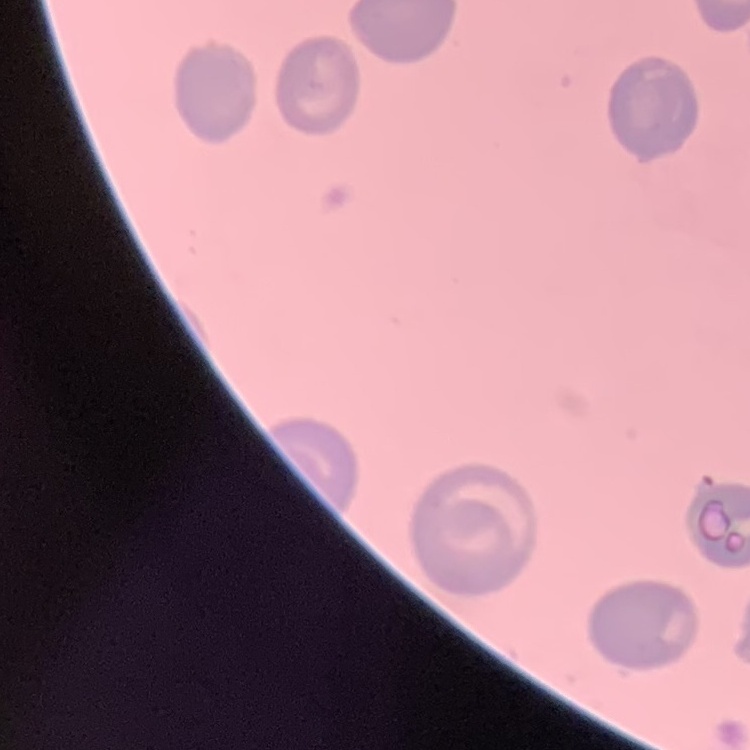 The red blood cells show no rouleaux formation. Square crop of a larger photomicrograph. Thin blood smear. Stained with either Field's or Giemsa.